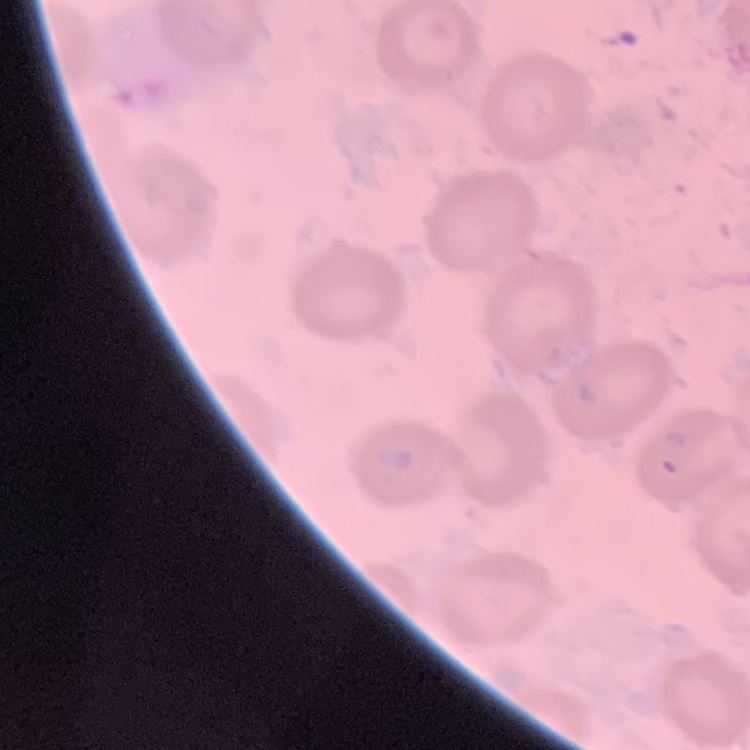
{
  "red_blood_cell_morphology": "no rouleaux formation",
  "preparation": "thin blood film",
  "image_type": "square crop of a larger photomicrograph",
  "stain": "Field's or Giemsa"
}